Assess this cell for malaria.
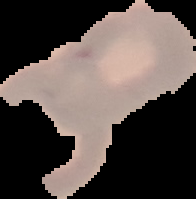
It is uninfected.

From a thin blood film. Image is 196×199 pixels. Cell region segmented out of the field of view; the surrounding area is masked to black.